Report the malaria status of this cell.
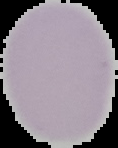

Uninfected.

image type = segmented cell region with the area outside set to black
image size = 118×148 pixels
preparation = thin blood smear